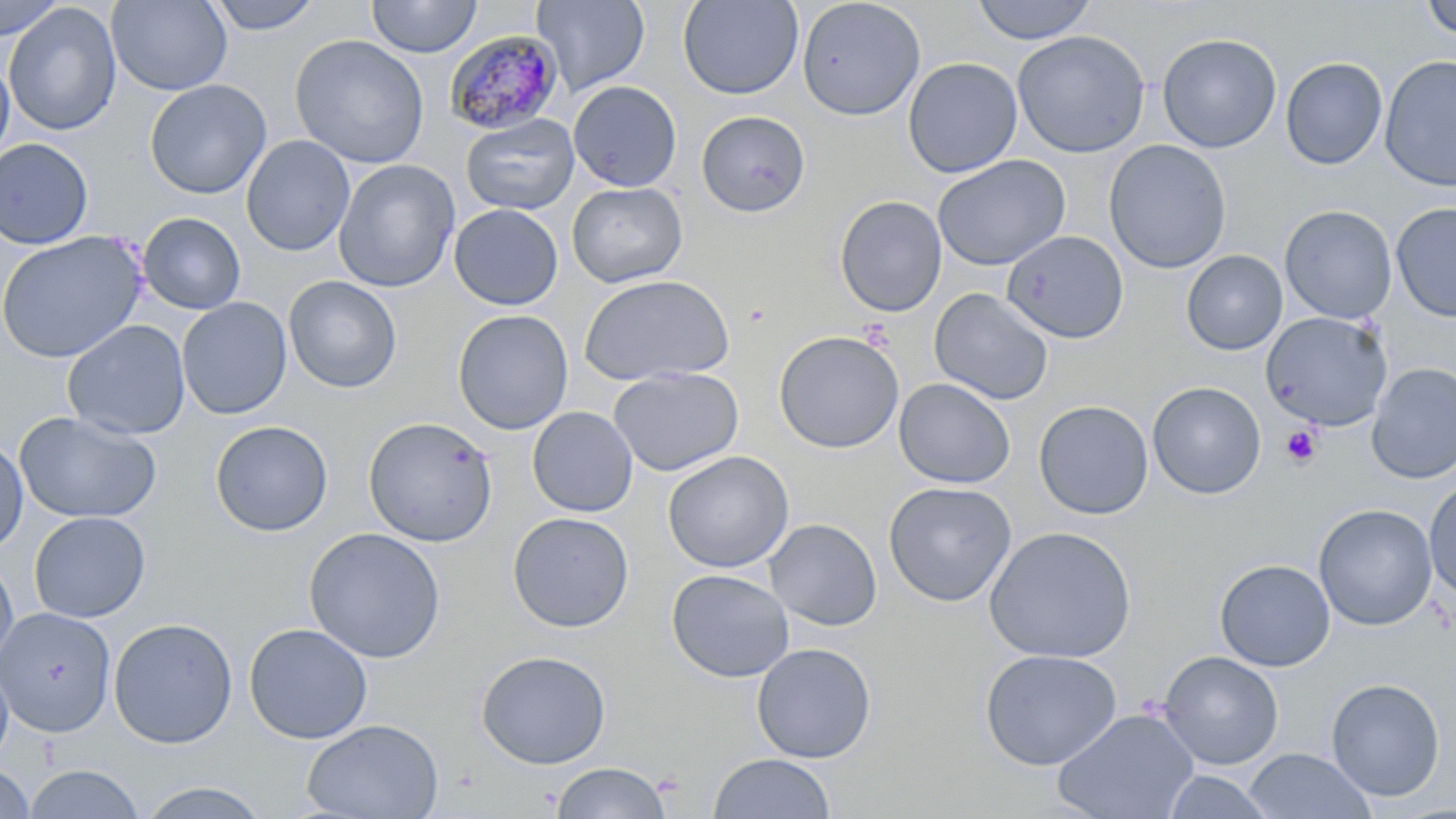

Summary:
  - Coordinate format: approximate bounding boxes as [x1, y1, x2, y2] in pixels
  - Platelet locations: [1280, 425, 1322, 467]
  - Uninfected red blood cell locations: [0, 0, 68, 40], [106, 0, 232, 95], [204, 0, 326, 35], [366, 0, 482, 58], [531, 0, 650, 96], [677, 0, 804, 100], [796, 0, 926, 121], [970, 0, 1097, 45], [1420, 0, 1456, 39], [3, 2, 122, 136], [1012, 30, 1150, 158], [1157, 33, 1282, 154], [289, 35, 430, 169], [1379, 54, 1456, 193], [0, 56, 15, 163], [1280, 57, 1388, 170], [903, 58, 1022, 178], [144, 79, 272, 200], [568, 81, 682, 192], [696, 110, 810, 217], [461, 114, 579, 214], [241, 135, 355, 256], [1, 138, 93, 249], [1103, 139, 1232, 274], [932, 154, 1070, 271], [333, 160, 459, 292], [567, 181, 688, 288], [833, 196, 947, 317], [1391, 202, 1455, 323], [449, 204, 563, 311], [1279, 205, 1397, 324], [138, 212, 246, 315], [1002, 230, 1129, 344], [0, 231, 146, 363], [1180, 250, 1288, 356], [578, 274, 735, 386], [283, 275, 401, 393], [928, 288, 1054, 406], [176, 297, 292, 419], [452, 309, 573, 434], [1260, 311, 1393, 431], [63, 320, 190, 440], [773, 330, 904, 453], [1366, 362, 1456, 484], [607, 366, 744, 477], [894, 378, 1015, 489], [1147, 381, 1267, 499], [1033, 399, 1154, 520], [527, 406, 638, 517], [15, 411, 161, 524], [363, 416, 499, 547], [210, 420, 333, 537], [0, 437, 28, 556], [662, 451, 794, 573], [1424, 477, 1456, 600], [883, 480, 1017, 607], [1313, 504, 1437, 631], [29, 511, 150, 623], [507, 512, 634, 633], [764, 519, 882, 631], [983, 526, 1137, 664], [304, 527, 446, 664], [0, 555, 19, 673], [1214, 559, 1335, 672], [666, 568, 795, 683], [0, 607, 115, 737], [108, 617, 238, 749], [244, 623, 373, 744], [751, 642, 877, 763], [979, 649, 1123, 770], [476, 650, 611, 769], [1158, 651, 1284, 770], [0, 658, 13, 765], [1326, 678, 1446, 801], [1052, 707, 1199, 819], [302, 719, 444, 819], [1244, 748, 1375, 819], [708, 753, 836, 818], [551, 762, 672, 819], [23, 763, 145, 819], [0, 764, 36, 818], [1161, 770, 1276, 818], [136, 781, 272, 818]
  - Plasmodium malariae-infected red blood cell locations: [444, 29, 563, 134]
  - Slide-level diagnosis: Plasmodium malariae
  - Field of view: single
  - Image size: 1456×819 pixels
  - Preparation: thin blood film
  - Magnification: 1000x
  - Modality: optical microscopy
  - Stain: May-Grünwald-Giemsa